Locate every blood parasite and identify its species.
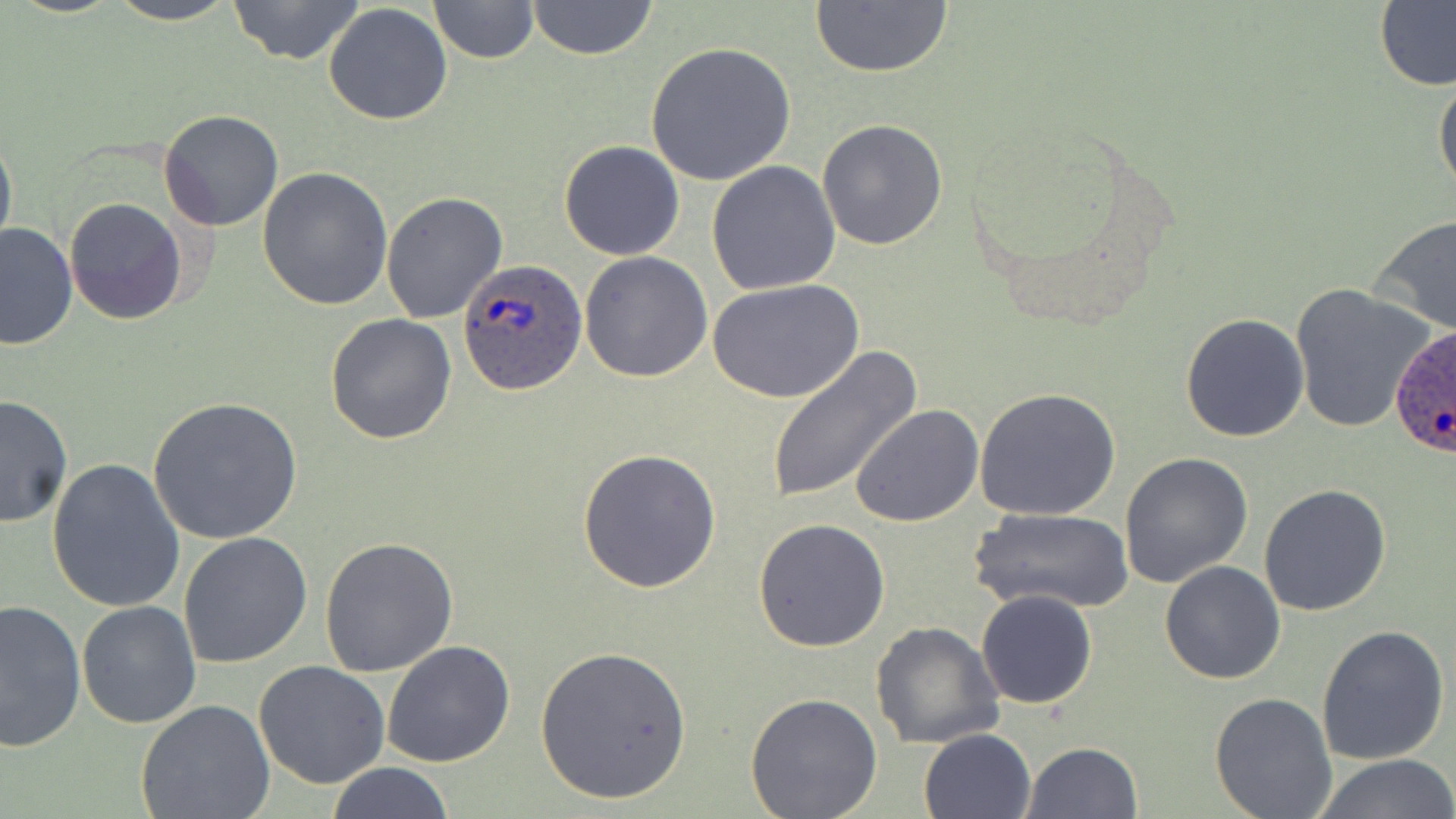
Approximate bounding boxes as (x1, y1, x2, y2) in pixels.
Plasmodium ovale-infected red blood cells: (459, 258, 588, 395), (1384, 318, 1452, 462).
No Plasmodium falciparum, Plasmodium malariae, Plasmodium vivax, Babesia divergens, or Trypanosoma brucei observed.

Summary:
  - Uninfected red blood cell locations: (102, 0, 244, 25), (226, 0, 366, 66), (428, 0, 539, 64), (527, 0, 657, 61), (809, 1, 953, 79), (1376, 2, 1456, 92), (323, 3, 453, 127), (644, 41, 797, 185), (1433, 69, 1456, 194), (158, 109, 284, 231), (817, 119, 949, 251), (0, 125, 17, 260), (558, 139, 686, 260), (706, 161, 841, 296), (257, 166, 392, 309), (381, 191, 509, 324), (64, 199, 186, 323), (1370, 214, 1456, 338), (0, 221, 77, 351), (579, 251, 713, 381), (709, 278, 863, 406), (1291, 283, 1436, 436), (325, 313, 457, 445), (1180, 314, 1309, 443), (765, 347, 918, 504), (972, 387, 1122, 522), (0, 394, 73, 528), (148, 396, 304, 546), (851, 405, 984, 528), (576, 449, 722, 594), (1119, 452, 1253, 587), (47, 456, 186, 613), (1258, 484, 1391, 616), (969, 506, 1136, 614), (755, 517, 890, 652), (178, 532, 312, 669), (318, 536, 459, 677), (1160, 559, 1287, 684), (975, 589, 1098, 709), (0, 597, 86, 750), (77, 600, 201, 730), (869, 621, 1004, 750), (1316, 625, 1449, 765), (382, 641, 516, 769), (532, 644, 694, 807), (253, 660, 390, 789), (140, 682, 387, 807), (745, 692, 882, 818), (1209, 692, 1337, 818), (136, 699, 275, 819), (919, 728, 1036, 819), (1023, 742, 1143, 818), (1311, 754, 1455, 819), (322, 762, 457, 819)
  - Slide-level diagnosis: Plasmodium ovale
  - Field of view: single
  - Modality: light microscopy
  - Preparation: thin blood film
  - Image size: 1456×819 pixels
  - Magnification: 1000x
  - Stain: May-Grünwald-Giemsa